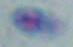
identification = Toxoplasma gondii
modality = micrograph
magnification = 1000x